Classify this cell by malaria status.
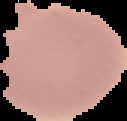

It is uninfected.

Summary:
  - Preparation: thin blood film
  - Image size: 127×121 pixels
  - Image type: cell region segmented out of the field of view; surrounding area masked to black